Assess the morphology of the red blood cells.
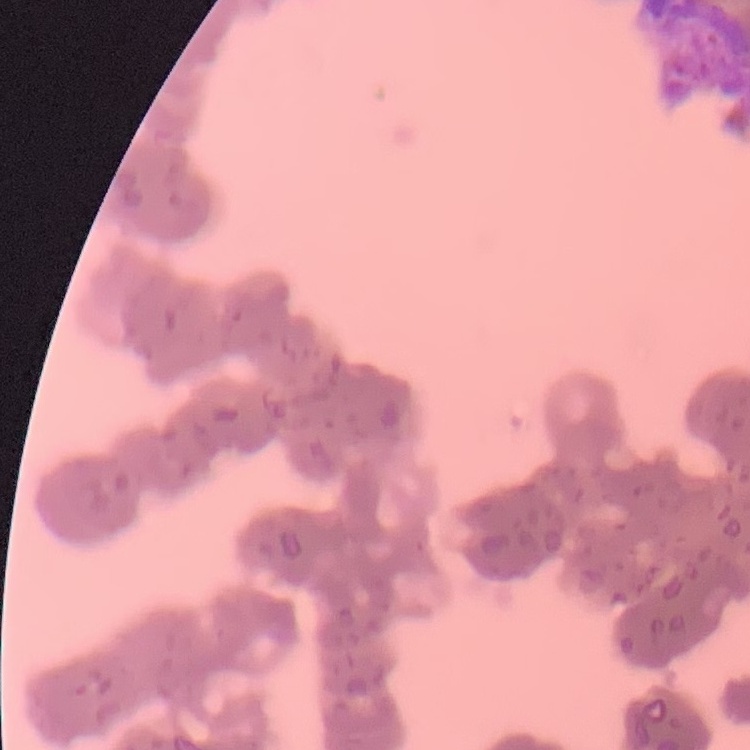
They show rouleaux formation.

{
  "image_type": "one tile cut from a larger photomicrograph",
  "stain": "Field's or Giemsa",
  "preparation": "thin blood film"
}